Give the position of every leukocyte visible.
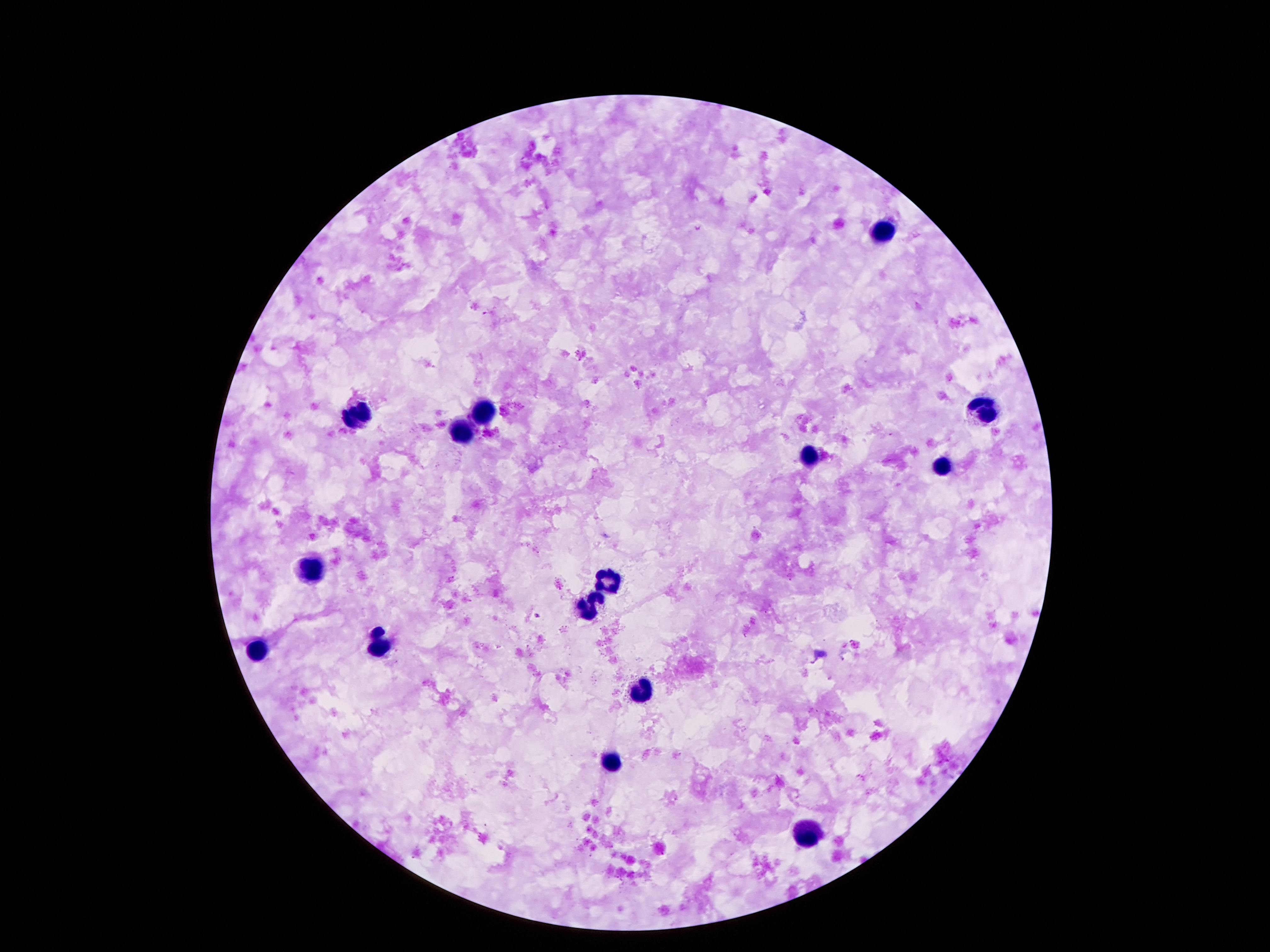
Approximate object centers, in pixels from the top-left corner.
Leukocytes: (x=883, y=231), (x=982, y=408), (x=482, y=413), (x=356, y=416), (x=462, y=433), (x=810, y=457), (x=945, y=466), (x=307, y=570), (x=606, y=581), (x=588, y=609), (x=380, y=647), (x=254, y=651), (x=639, y=691), (x=611, y=760), (x=807, y=834).

field of view = one from this slide
magnification = 100x
capture = smartphone camera through the microscope eyepiece
image size = 1270×952 pixels
preparation = thick blood smear
patient malaria status = negative
stain = Giemsa